Report the malaria status of this cell.
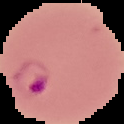
It is parasitized.

Image is 124×124 pixels. Cell region segmented out of the field of view; the surrounding area is masked to black. From a thin blood film.